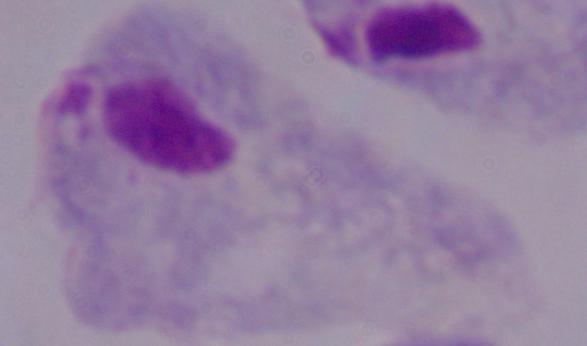
Summary:
  - Identification: trichomonad
  - Magnification: 1000x
  - Modality: photomicrograph